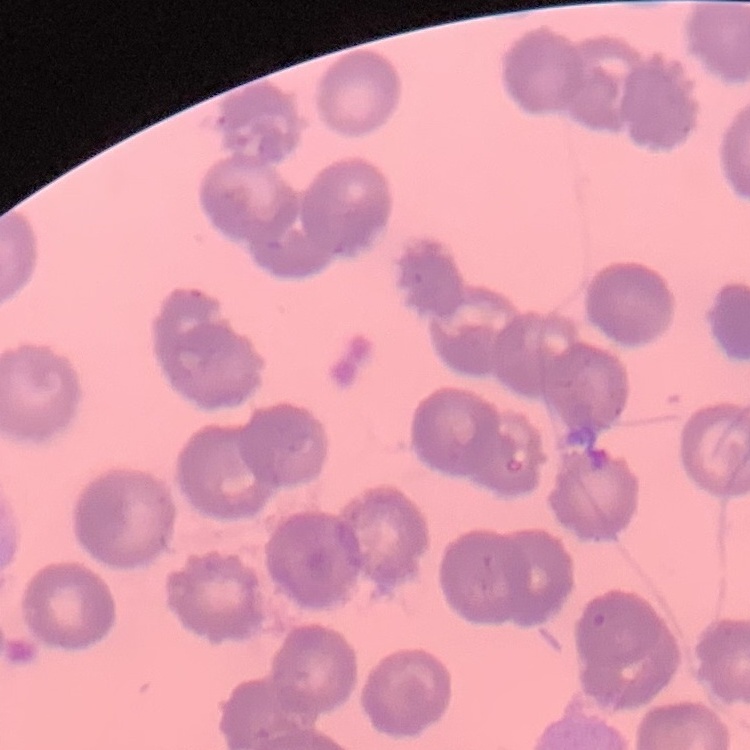

The red blood cells exhibit no rouleaux formation. Thin blood film. Square crop of a larger photomicrograph. Field's or Giemsa stain.